Identify the blood parasite species.
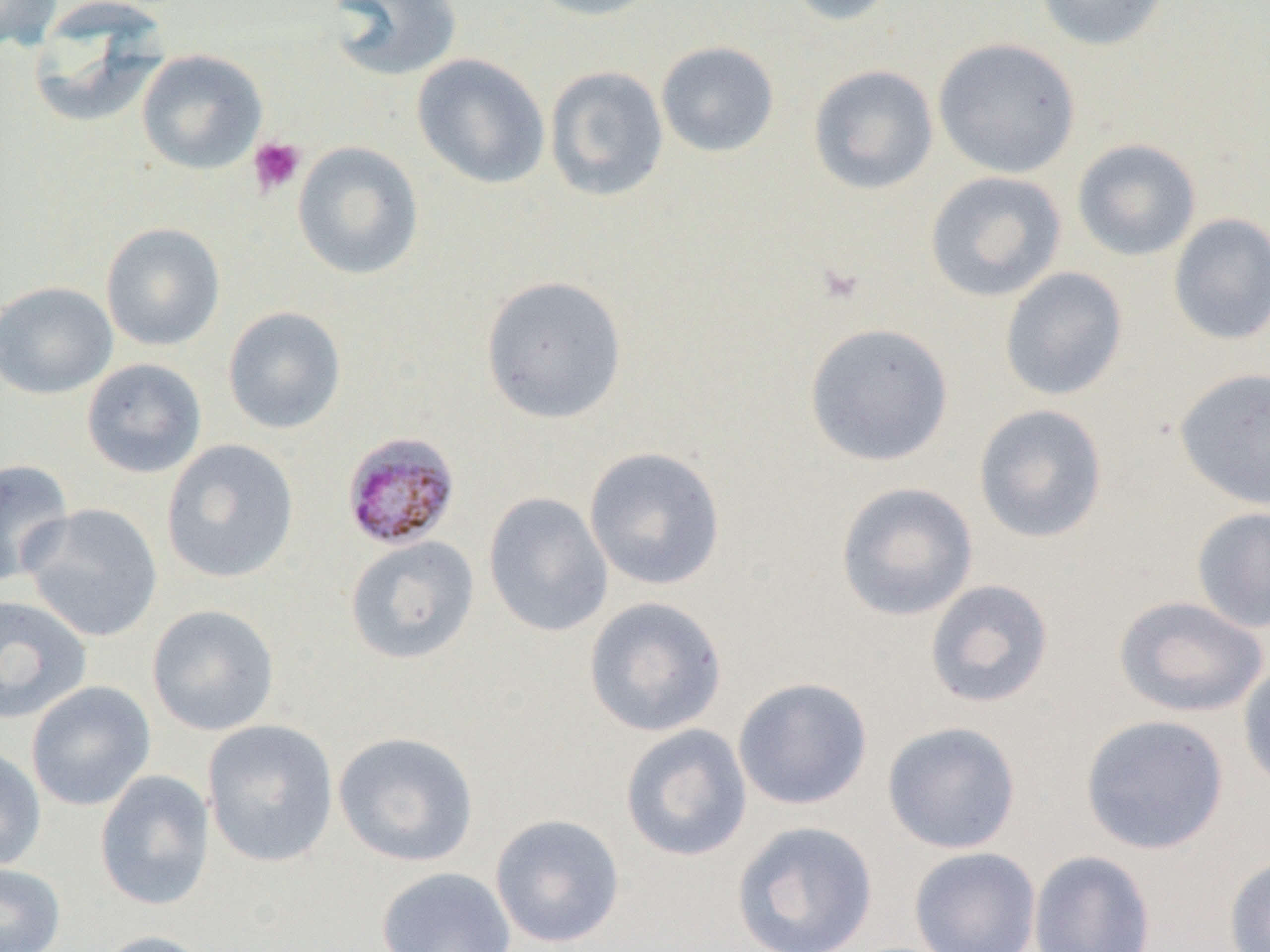

Plasmodium malariae.

field of view = one of a larger specimen
uninfected red blood cell locations = approximate bounding boxes as (x1,y1)-(x2,y2) corner pairs in pixels: (0,0)-(62,52), (324,0)-(463,82), (524,0)-(667,21), (783,0)-(901,26), (1035,0)-(1170,51), (28,2)-(169,127), (933,38)-(1081,178), (655,41)-(780,158), (136,50)-(268,175), (411,54)-(550,190), (544,65)-(669,202), (807,65)-(939,196), (1071,138)-(1202,261), (292,141)-(424,281), (924,170)-(1067,303), (1168,213)-(1270,346), (100,222)-(226,351), (999,267)-(1128,401), (480,274)-(628,424), (0,280)-(118,400), (222,306)-(347,434), (803,322)-(954,467), (81,358)-(207,479), (1173,367)-(1270,510), (973,403)-(1108,544), (160,439)-(299,584), (583,446)-(726,591), (0,458)-(75,587), (835,481)-(979,622), (483,492)-(613,638), (21,503)-(164,644), (1191,505)-(1270,634), (344,535)-(480,665), (924,579)-(1054,709), (0,594)-(92,724), (1114,595)-(1268,718), (583,596)-(728,737), (146,604)-(280,736), (1238,657)-(1270,794), (732,677)-(873,811), (26,680)-(156,812), (1079,713)-(1230,855), (201,719)-(339,867), (882,721)-(1022,854), (620,724)-(753,862), (332,731)-(480,867), (0,744)-(47,872), (94,770)-(215,911), (490,813)-(626,948), (730,820)-(879,952), (908,846)-(1041,952), (1027,849)-(1157,952), (1223,853)-(1270,952), (1,862)-(65,952), (376,866)-(517,952), (91,930)-(217,952)
preparation = thin blood film
image size = 1270×952 pixels
magnification = 1000x
modality = light microscopy
platelet locations = approximate bounding boxes as (x1,y1)-(x2,y2) corner pairs in pixels: (247,136)-(306,197), (816,261)-(867,306)
Plasmodium malariae-infected red blood cell locations = approximate bounding boxes as (x1,y1)-(x2,y2) corner pairs in pixels: (341,431)-(461,551)